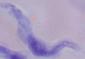
Micrograph. A trypanosome is shown. Captured at 1000x magnification.